Name the parasite shown.
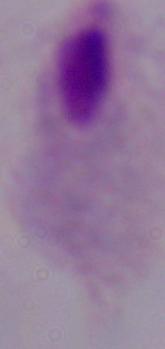
This is a trichomonad.

Summary:
  - Modality: micrograph
  - Magnification: 1000x